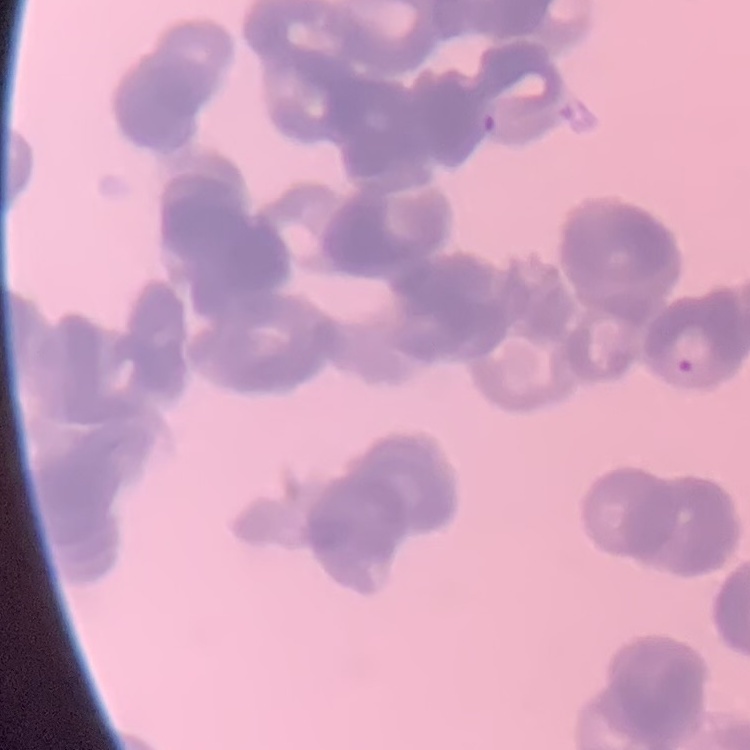 The red blood cells show rouleaux formation. Field's or Giemsa stain. Thin blood smear. Square crop of a larger photomicrograph.